Classify this cell by malaria status.
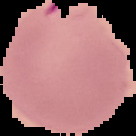

It is parasitized.

Summary:
  - Image size: 136×136 pixels
  - Image type: segmented cell region on a black background
  - Preparation: thin blood smear